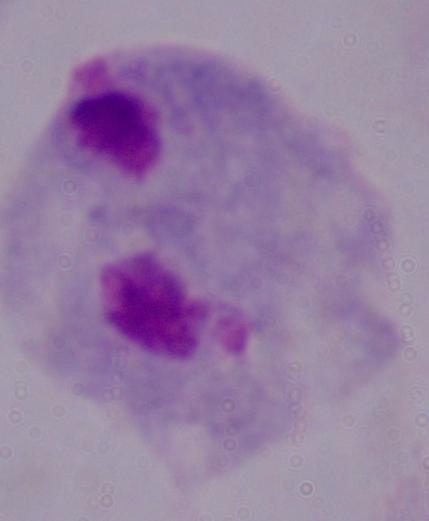
modality: micrograph
magnification: 1000x
identification: trichomonad